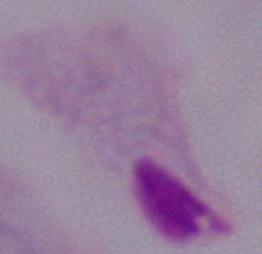
identification = trichomonad
magnification = 1000x
modality = micrograph